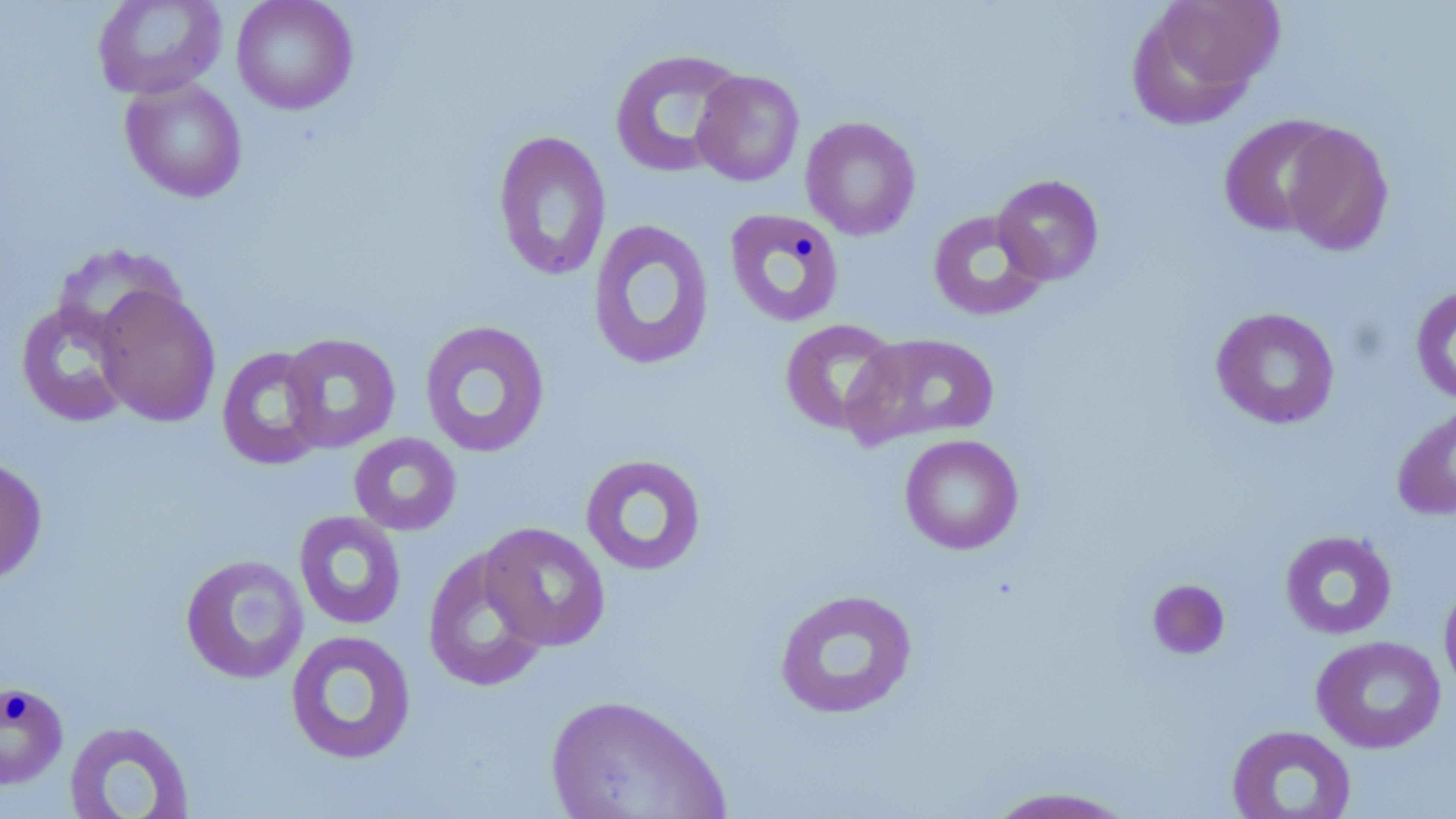
slide-level diagnosis = no evidence of blood parasites
field of view = single
image size = 1456×819 pixels
preparation = thin blood smear
stain = May-Grünwald-Giemsa
magnification = 1000x
modality = optical microscopy
uninfected red blood cell locations = approximate bounding boxes as [x1, y1, x2, y2] in pixels: [92, 0, 227, 100], [231, 0, 358, 115], [1127, 0, 1280, 129], [609, 48, 746, 178], [692, 70, 804, 187], [119, 77, 248, 203], [1218, 115, 1344, 237], [800, 116, 921, 241], [1280, 123, 1395, 256], [492, 129, 612, 283], [992, 174, 1104, 285], [724, 207, 845, 328], [927, 209, 1050, 321], [587, 218, 715, 371], [92, 284, 221, 427], [1410, 284, 1456, 406], [14, 298, 138, 427], [1210, 306, 1340, 430], [779, 318, 904, 436], [419, 320, 550, 458], [844, 330, 1001, 449], [280, 332, 401, 453], [217, 346, 329, 471], [1391, 403, 1456, 521], [348, 432, 462, 536], [899, 434, 1024, 554], [579, 453, 708, 576], [0, 455, 49, 586], [294, 510, 407, 630], [479, 521, 612, 651], [1279, 530, 1398, 640], [421, 548, 551, 693], [180, 554, 308, 684], [1146, 578, 1231, 660], [1439, 579, 1456, 700], [773, 587, 918, 720], [285, 629, 418, 765], [1310, 635, 1447, 753], [0, 681, 69, 791], [545, 693, 730, 818], [63, 719, 195, 819], [1226, 725, 1357, 819], [979, 785, 1141, 818]